Name the parasite shown.
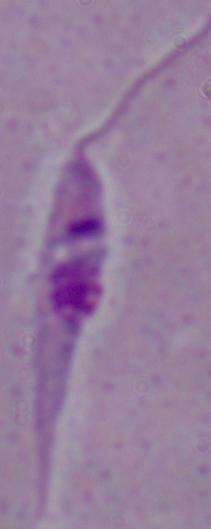
Leishmania.

Summary:
  - Magnification: 1000x
  - Modality: photomicrograph